Classify this cell by malaria status.
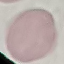
Uninfected.

capture: smartphone through the microscope eyepiece
preparation: thin blood film
image_type: automatically extracted cell patch, resized to 64 × 64 pixels
stain: Giemsa